Locate every malaria parasite.
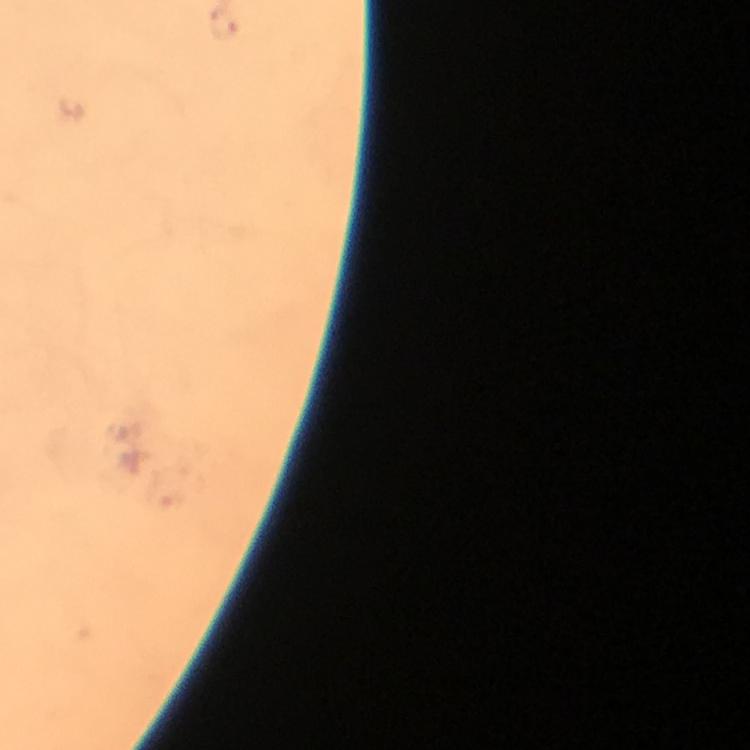

Approximate centers as [x, y] in pixels.
Malaria parasites: [226, 26].

Thick blood film. Giemsa stain. Image is 750×750 pixels. Cropped region of a single field of view. At 100x magnification. Immersion oil applied. Photographed through the microscope with a smartphone camera. From a malaria diagnostic workup.